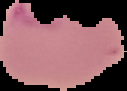
Image is 127×91 pixels. Malaria status: parasitized. From a thin blood film. Segmented cell region on a black background.